Classify this cell by malaria status.
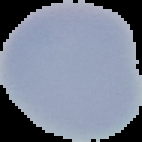

It is uninfected.

From a thin blood film. Image is 142×142 pixels. The area outside the segmented cell region is set to black.